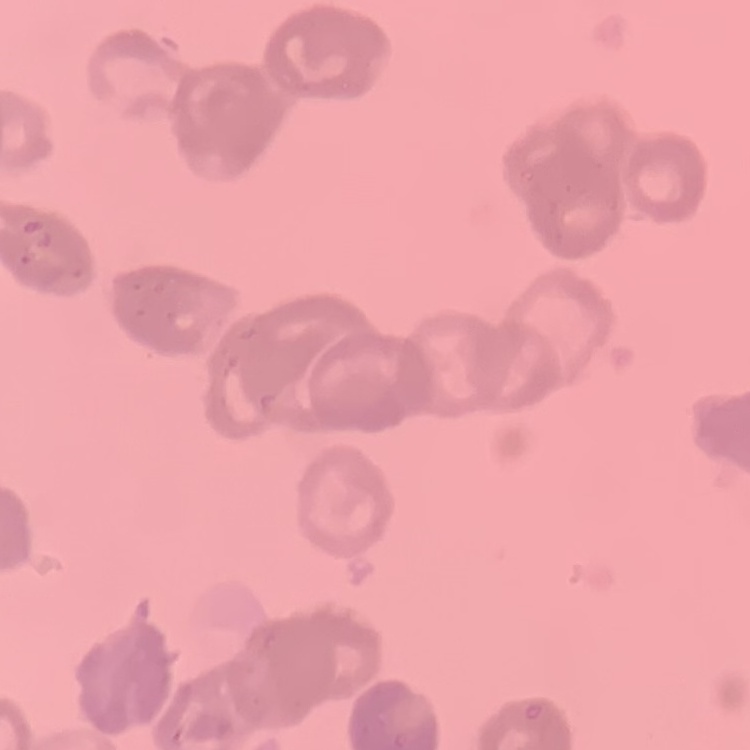
The red blood cells exhibit rouleaux formation. Square crop of a larger photomicrograph. Thin peripheral smear. Stained with either Field's or Giemsa.